Classify this cell by malaria status.
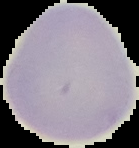
It is uninfected.

Image is 139×148 pixels. The area outside the segmented cell region is set to black. From a thin blood film.